Assess the morphology of the red blood cells.
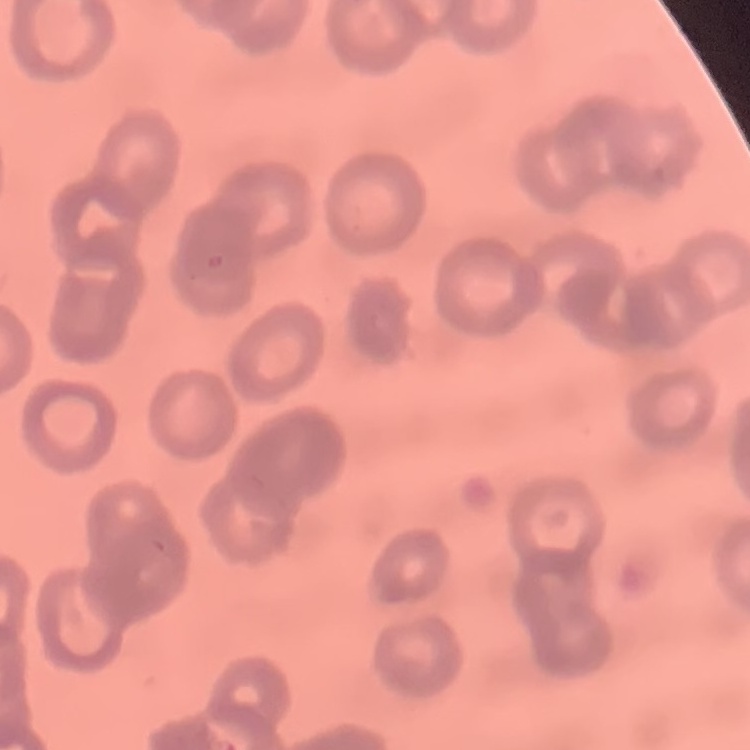

Rouleaux formation.

stain = Field's or Giemsa
preparation = thin peripheral smear
image type = square crop of a larger photomicrograph